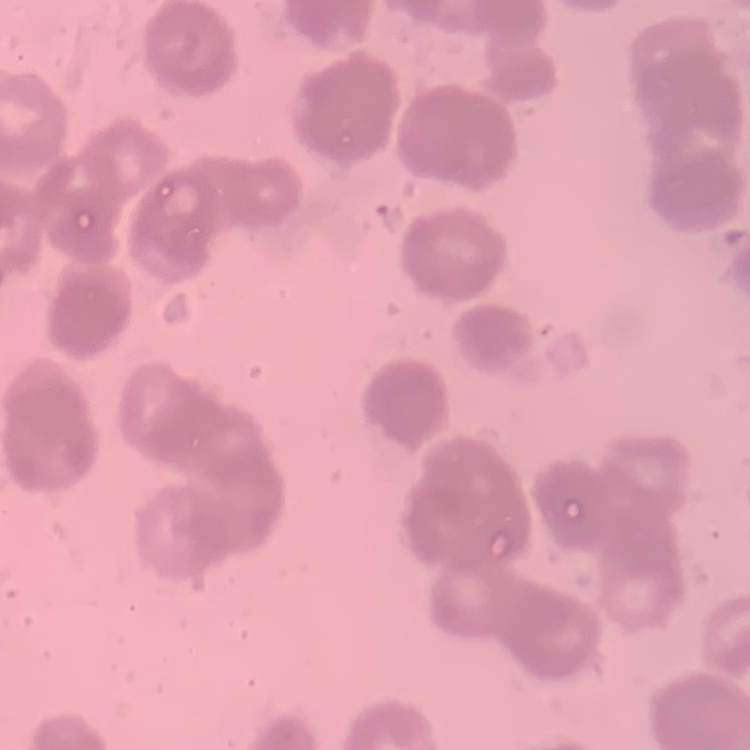

Summary:
  - Erythrocyte morphology: rouleaux formation
  - Preparation: thin blood film
  - Image type: square crop of a larger photomicrograph
  - Stain: Field's or Giemsa